Comment on the morphology of the red blood cells.
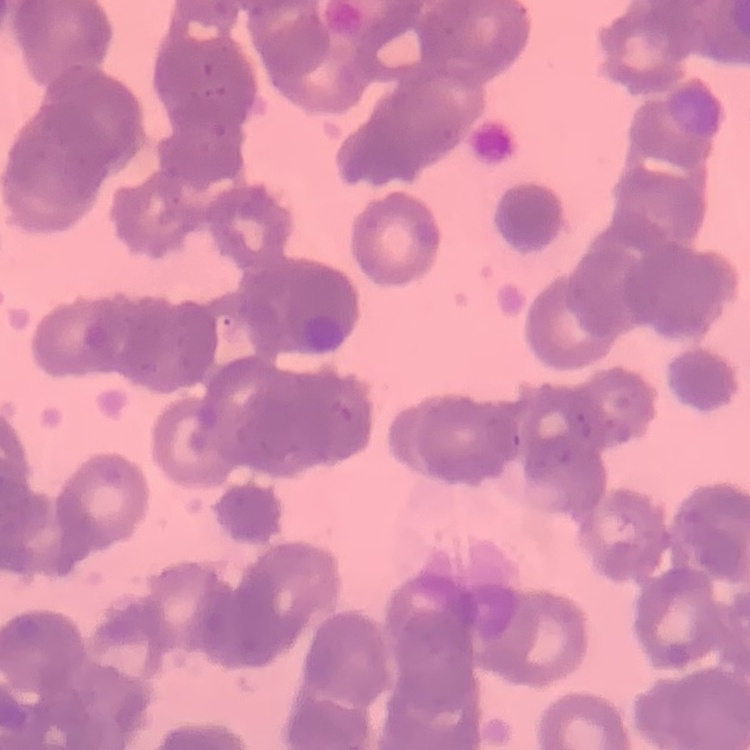
Rouleaux formation.

Summary:
  - Preparation: thin blood smear
  - Image type: square crop of a larger photomicrograph
  - Stain: Field's or Giemsa